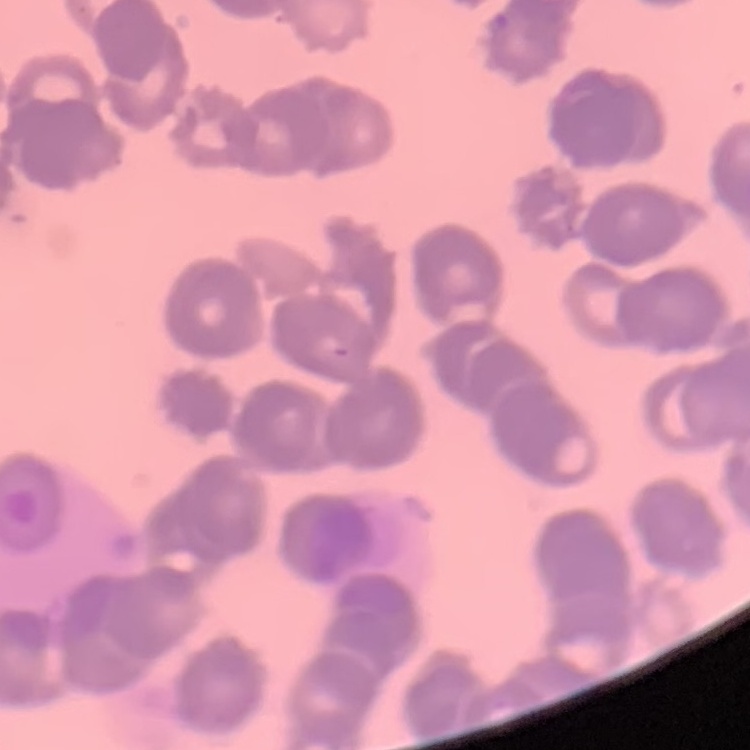

red_blood_cell_morphology: rouleaux formation
stain: Field's or Giemsa
image_type: one tile cut from a larger photomicrograph
preparation: thin peripheral smear